Give the extent of all uninfected red blood cells.
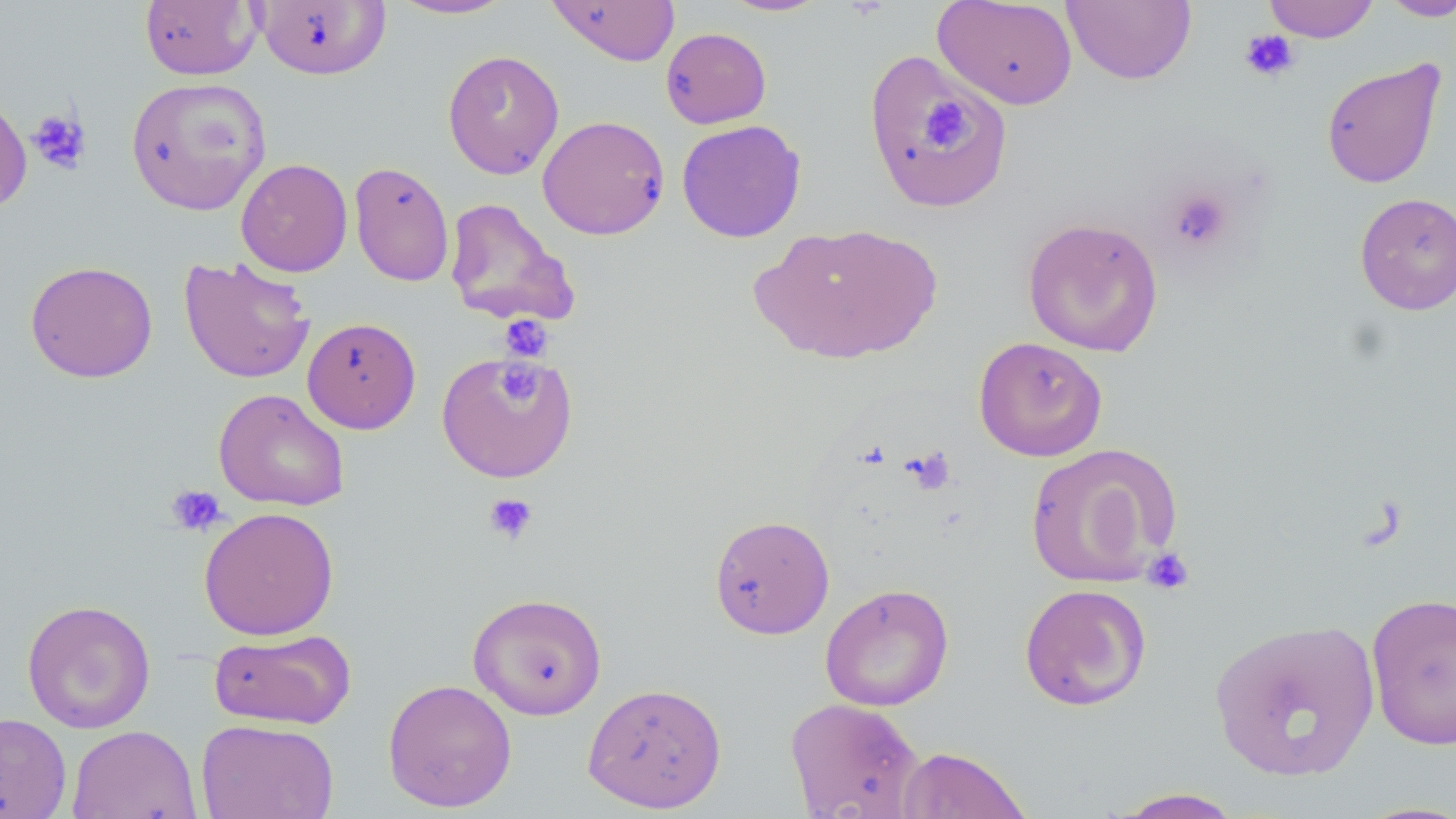

Approximate bounding boxes as (x1, y1, x2, y2) in pixels.
Uninfected red blood cells: (139, 0, 260, 80), (253, 0, 391, 81), (387, 0, 517, 20), (545, 0, 682, 66), (718, 0, 831, 17), (933, 0, 1078, 109), (1062, 0, 1196, 85), (1262, 0, 1380, 42), (1378, 0, 1456, 22), (660, 27, 772, 128), (862, 48, 1010, 211), (443, 49, 564, 179), (1321, 58, 1446, 189), (126, 77, 272, 216), (0, 88, 32, 215), (537, 114, 670, 240), (676, 120, 806, 243), (235, 158, 353, 277), (349, 160, 455, 287), (1355, 192, 1456, 315), (443, 197, 580, 329), (1022, 216, 1164, 357), (754, 221, 943, 364), (178, 255, 315, 384), (25, 260, 158, 383), (302, 317, 421, 434), (973, 336, 1108, 462), (436, 350, 578, 483), (213, 388, 350, 511), (1024, 443, 1179, 587), (198, 506, 339, 640), (709, 514, 835, 639), (819, 583, 954, 711), (1019, 583, 1152, 711), (1365, 591, 1456, 749), (467, 592, 607, 720), (21, 599, 156, 734), (1208, 618, 1380, 782), (207, 627, 357, 731), (382, 678, 518, 812), (582, 681, 727, 813), (784, 696, 924, 819), (0, 712, 72, 819), (197, 718, 340, 819), (67, 725, 202, 819), (896, 746, 1032, 819), (1111, 788, 1245, 818).

slide_level_diagnosis: no evidence of blood parasites
stain: May-Grünwald-Giemsa
magnification: 1000x
preparation: thin blood film
modality: optical microscopy
image_size: 1456×819 pixels
platelet_locations: 'approximate bounding boxes as (x1, y1, x2, y2) in pixels: (1239, 29, 1300, 82), (920, 97, 968, 149), (27, 108, 93, 175), (1166, 186, 1233, 252), (498, 314, 554, 363), (500, 362, 536, 404), (904, 447, 956, 496), (165, 484, 227, 537), (483, 493, 538, 546), (1141, 548, 1194, 595)'
field_of_view: single